Comment on the morphology of the red blood cells.
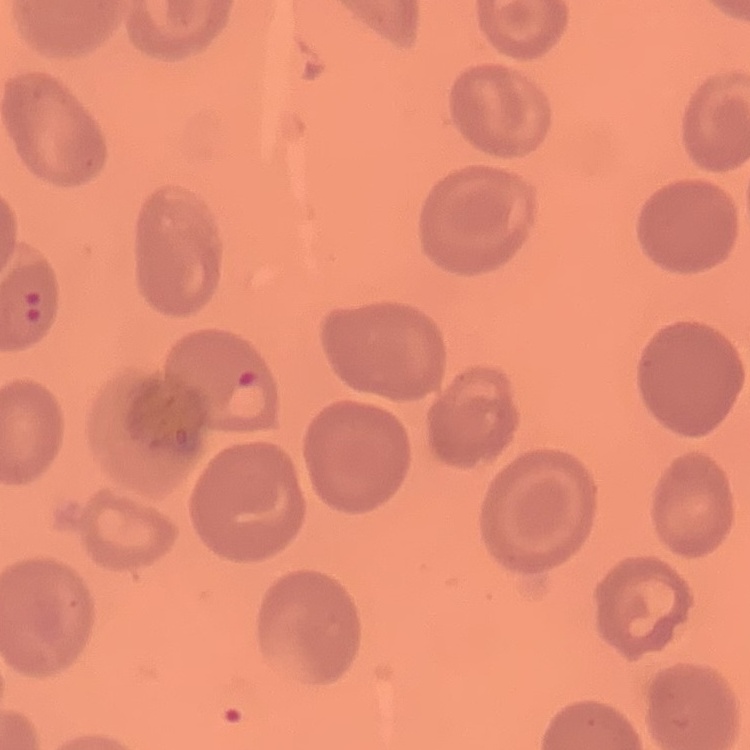

No rouleaux formation.

Summary:
  - Image type: square crop of a larger photomicrograph
  - Preparation: thin peripheral smear
  - Stain: Field's or Giemsa